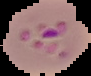
Summary:
  - Image size: 91×76 pixels
  - Malaria status: parasitized
  - Preparation: thin blood film
  - Image type: segmented cell region with the area outside set to black